Assess this cell for malaria.
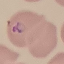
Parasitized.

Thin blood film. Giemsa stain. Photographed with a smartphone camera at the microscope eyepiece. Automatically extracted cell patch, resized to 64 × 64 pixels.